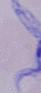

Photomicrograph. A trypanosome is seen. Captured at 1000x magnification.